Mark where platelets are.
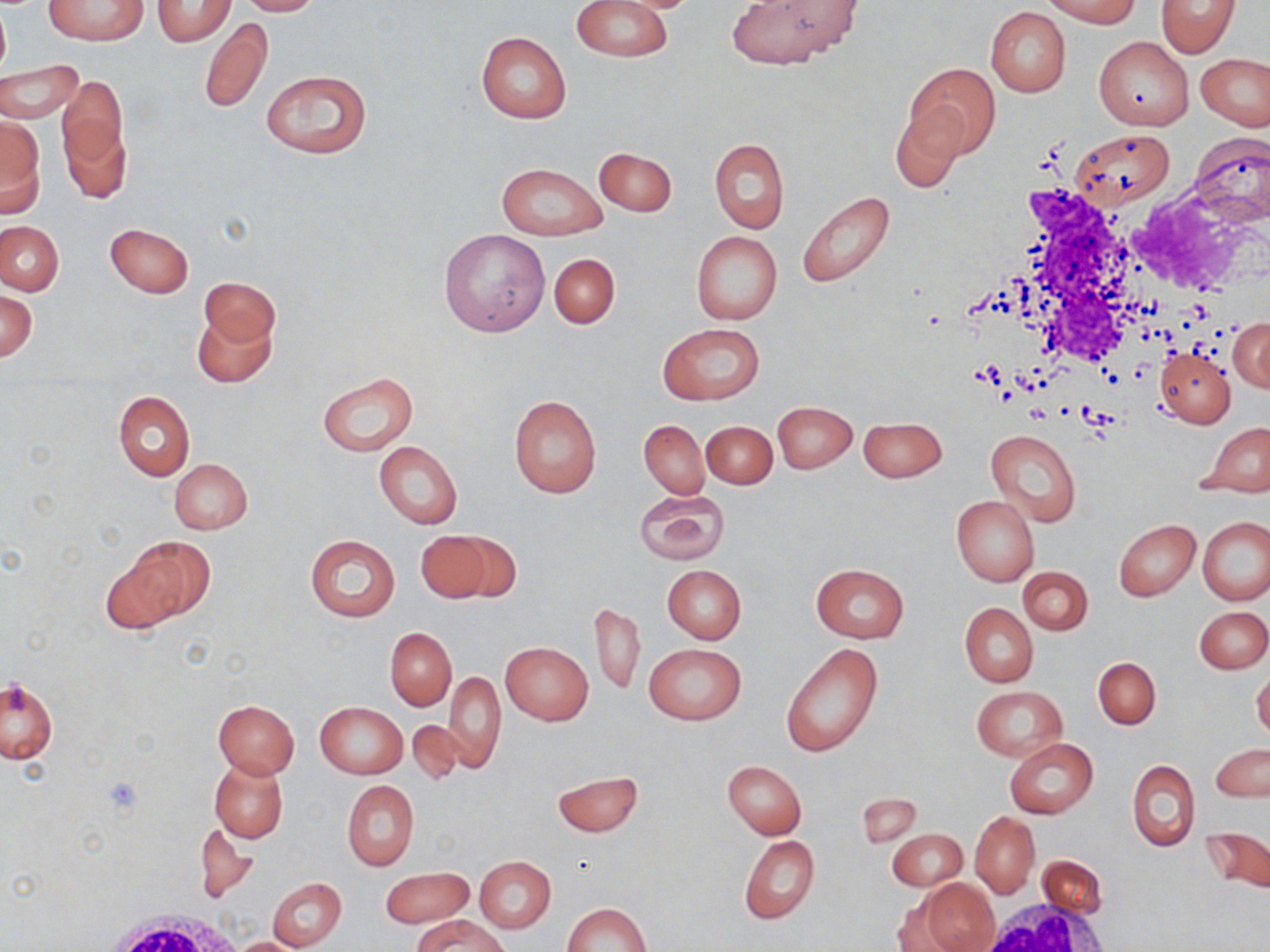
Approximate bounding boxes as (x1, y1, x2, y2) in pixels.
Platelets: (101, 775, 144, 816).

Uninfected red blood cell locations: (43, 0, 147, 44), (237, 0, 323, 16), (573, 0, 671, 62), (727, 0, 860, 68), (1044, 0, 1140, 26), (1155, 0, 1240, 56), (151, 1, 236, 45), (0, 2, 10, 83), (986, 7, 1070, 96), (198, 18, 272, 114), (476, 31, 572, 123), (1093, 37, 1193, 131), (1195, 53, 1269, 131), (0, 61, 83, 122), (905, 63, 999, 158), (260, 70, 371, 160), (57, 74, 128, 180), (890, 110, 964, 194), (0, 115, 44, 215), (60, 118, 134, 206), (1069, 130, 1176, 208), (1189, 133, 1270, 225), (708, 139, 789, 234), (593, 147, 678, 216), (496, 162, 607, 241), (796, 192, 897, 287), (0, 221, 65, 295), (105, 222, 194, 297), (438, 229, 551, 336), (690, 231, 782, 325), (548, 253, 620, 329), (200, 277, 279, 350), (1, 291, 37, 361), (193, 308, 276, 388), (1230, 318, 1270, 391), (658, 323, 764, 405), (1155, 348, 1236, 427), (317, 372, 419, 455), (112, 391, 195, 480), (509, 394, 601, 497), (773, 402, 857, 474), (858, 416, 946, 482), (639, 419, 708, 498), (702, 421, 777, 489), (1199, 422, 1270, 496), (986, 430, 1081, 525), (374, 441, 463, 530), (169, 459, 252, 534), (634, 489, 729, 565), (951, 496, 1039, 586), (1198, 517, 1269, 605), (1114, 519, 1200, 600), (415, 530, 500, 603), (305, 534, 399, 623), (124, 535, 213, 622), (99, 552, 184, 634), (812, 563, 909, 642), (662, 565, 746, 645), (1019, 567, 1092, 635), (590, 603, 645, 698), (959, 603, 1037, 687), (1195, 607, 1269, 674), (385, 627, 456, 712), (500, 642, 593, 726), (779, 642, 883, 758), (645, 644, 745, 725), (1093, 657, 1160, 729), (442, 670, 507, 771), (1252, 670, 1270, 741), (1, 677, 57, 764), (972, 687, 1065, 760), (213, 700, 300, 779), (315, 702, 407, 779), (405, 719, 473, 785), (1005, 737, 1098, 819), (1211, 743, 1269, 800), (210, 758, 288, 842), (723, 760, 806, 839), (1128, 760, 1200, 851), (553, 770, 643, 837), (341, 781, 419, 871), (971, 812, 1040, 897), (193, 823, 258, 902), (1200, 826, 1270, 896), (885, 827, 968, 892), (739, 835, 819, 925), (1034, 855, 1108, 919), (474, 856, 556, 932), (379, 866, 474, 929), (267, 877, 346, 951), (915, 878, 998, 952), (563, 902, 649, 951), (416, 915, 510, 952), (232, 936, 307, 951). White blood cell locations: (1000, 179, 1169, 373), (89, 898, 246, 952). Slide-level diagnosis: no evidence of blood parasites. Single field of view. Thin blood film. May-Grünwald-Giemsa stain. Optical microscopy. Captured at 1000x magnification. Image is 1270×952 pixels.